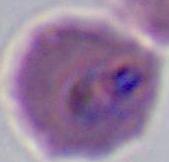

Photomicrograph. A Plasmodium parasite is seen. 400x or 1000x magnification.